Give the extent of all uninfected red blood cells.
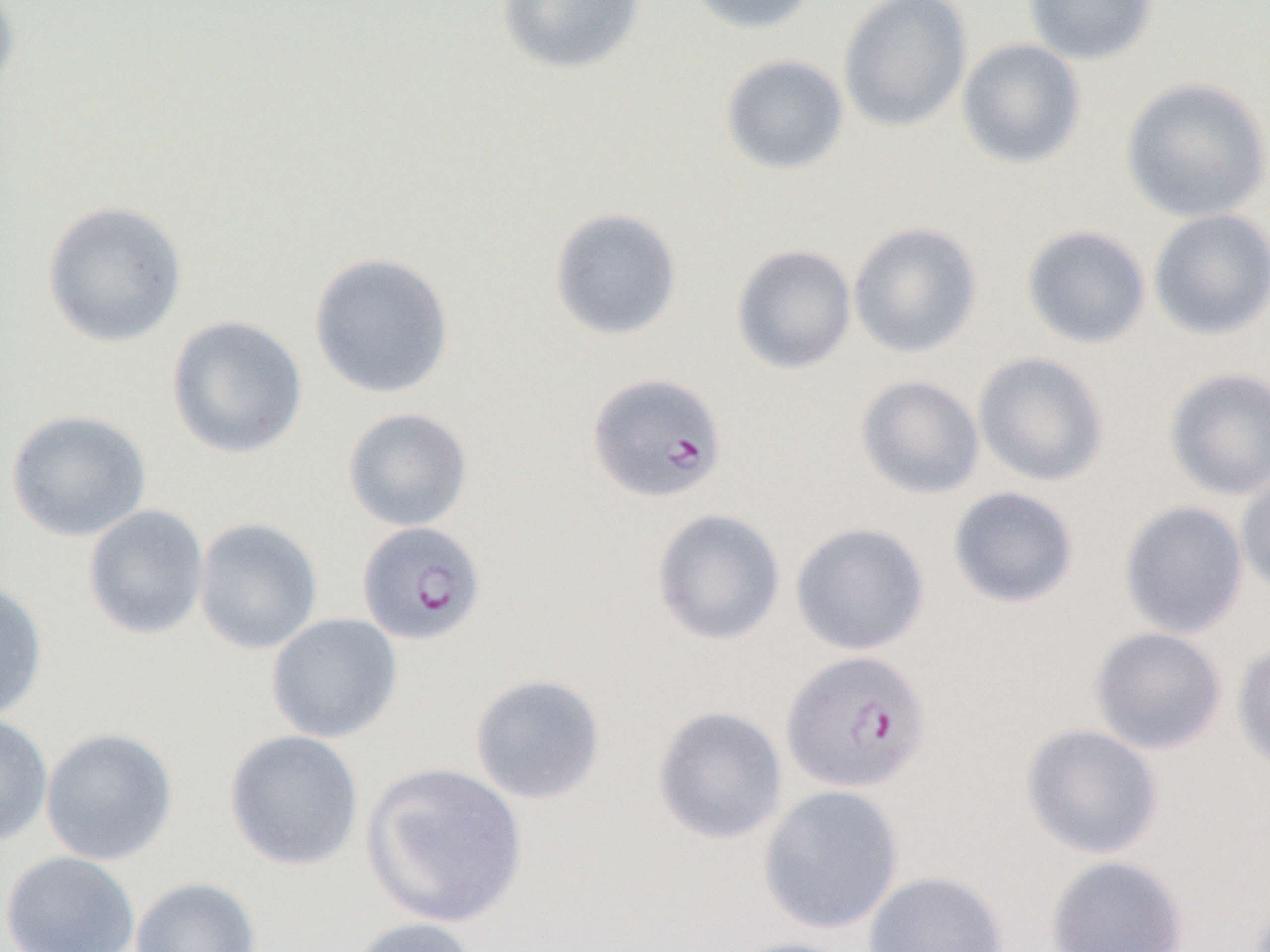

Approximate bounding boxes as [x1, y1, x2, y2] in pixels.
Uninfected red blood cells: [496, 0, 646, 76], [684, 0, 822, 35], [838, 0, 973, 133], [1025, 0, 1158, 66], [0, 1, 22, 102], [956, 38, 1086, 169], [720, 54, 849, 176], [1120, 77, 1270, 224], [42, 200, 188, 348], [548, 207, 683, 341], [1148, 208, 1270, 341], [848, 221, 983, 358], [1021, 225, 1151, 349], [731, 244, 857, 374], [308, 251, 455, 399], [166, 315, 308, 459], [973, 352, 1110, 487], [1164, 367, 1270, 501], [855, 375, 986, 499], [342, 407, 473, 532], [5, 409, 152, 542], [1236, 470, 1270, 596], [947, 485, 1080, 609], [1119, 500, 1249, 639], [83, 504, 210, 640], [651, 507, 786, 645], [193, 517, 324, 655], [790, 521, 930, 656], [0, 580, 49, 722], [266, 613, 403, 744], [1089, 626, 1227, 755], [1232, 638, 1270, 775], [470, 674, 606, 805], [652, 705, 788, 845], [0, 712, 54, 847], [1019, 723, 1164, 859], [40, 727, 179, 866], [223, 729, 365, 871], [361, 761, 528, 928], [758, 784, 904, 935], [1, 849, 140, 952], [1045, 854, 1189, 951], [862, 870, 1008, 952], [129, 875, 263, 952], [345, 916, 481, 952], [723, 936, 862, 952].

Plasmodium falciparum-infected red blood cell locations = approximate bounding boxes as [x1, y1, x2, y2] in pixels: [588, 373, 727, 502], [356, 521, 486, 646], [780, 650, 932, 794]
slide-level diagnosis = Plasmodium falciparum
preparation = thin blood film
field of view = one of a larger specimen
modality = optical microscopy
image size = 1270×952 pixels
magnification = 1000x